Identify the parasite.
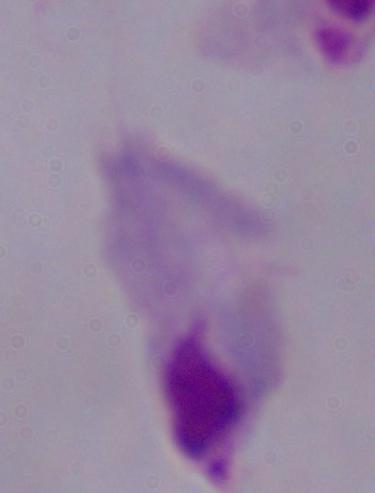

A trichomonad.

Photomicrograph. 1000x magnification.